Point out each Plasmodium parasite and each leukocyte.
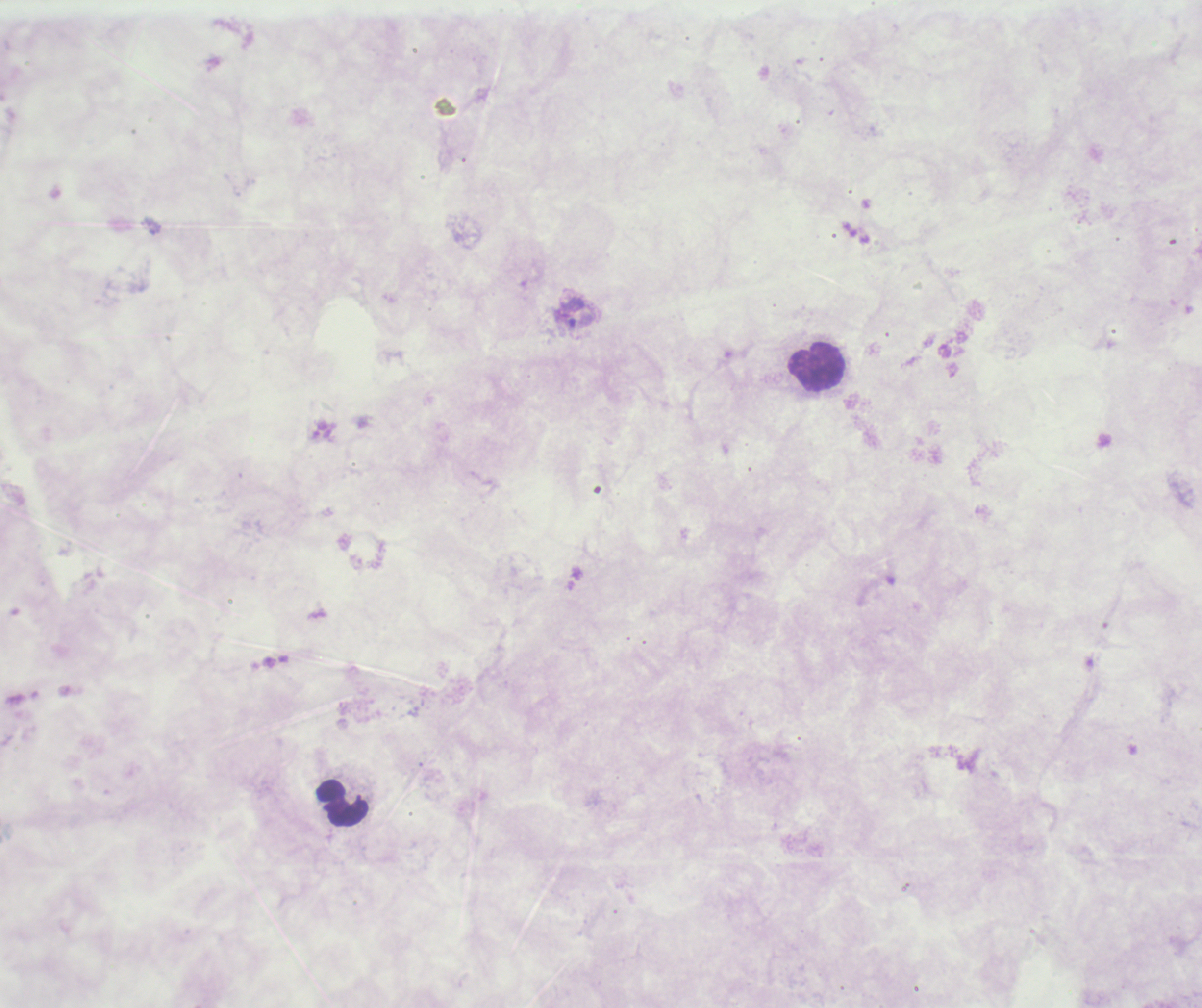

Approximate centers as (x, y) in pixels.
Trophozoites: (579, 321).
No schizont or gametocyte forms observed.
Leukocytes: (816, 367), (341, 803).

Summary:
  - Coloration quality: bad
  - Magnification: 100x
  - Context: previously used in a real diagnosis
  - Preparation: thick blood smear
  - Background quality: unsatisfactory
  - Image size: 1202×1008 pixels
  - Field of view: one from this slide
  - Stain: Romanowsky